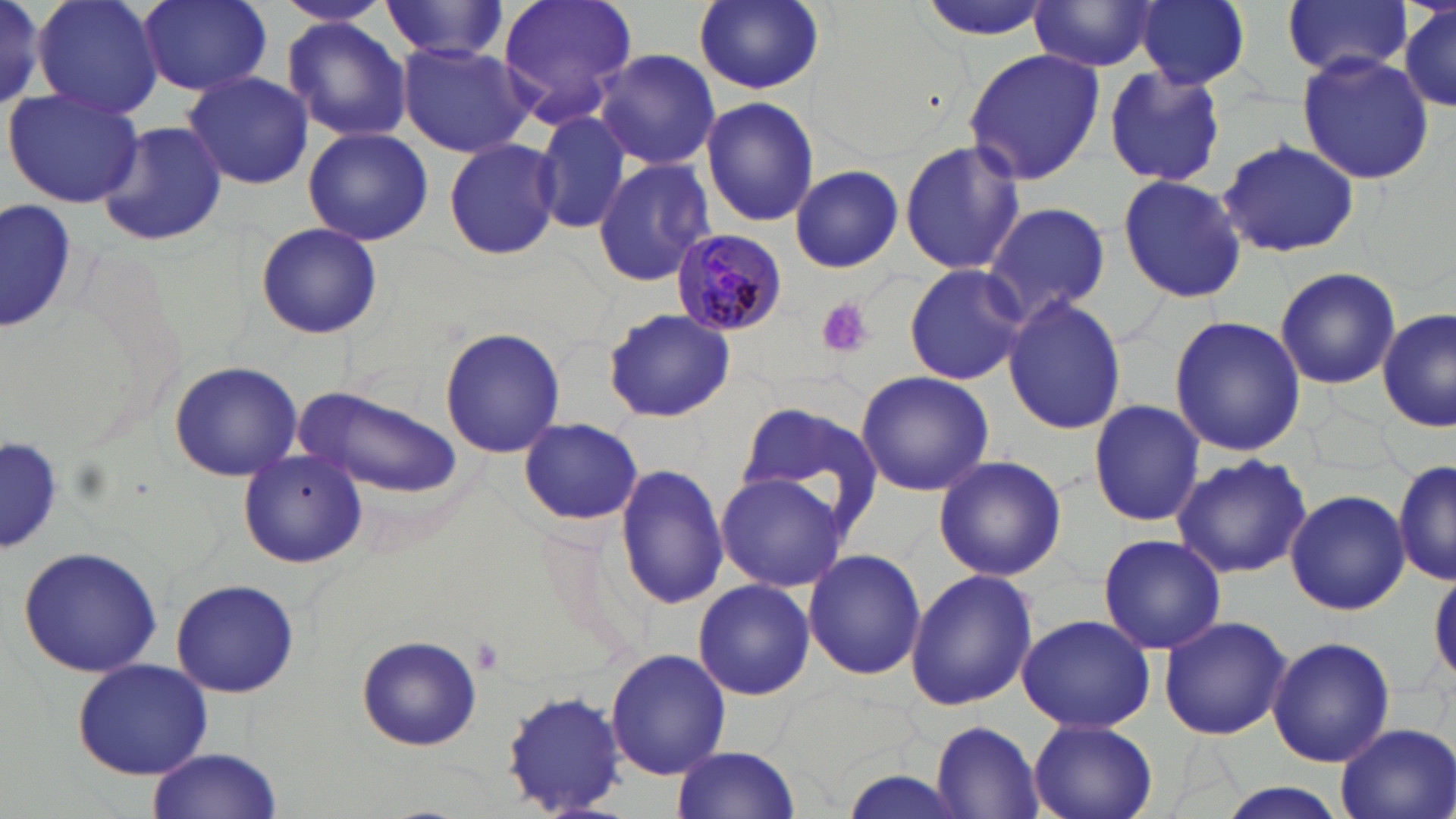 Approximate bounding boxes as [x1, y1, x2, y2] in pixels. Plasmodium malariae-infected red blood cell locations: [669, 230, 788, 338]. Uninfected red blood cell locations: [35, 0, 163, 121], [138, 0, 272, 95], [272, 0, 394, 31], [498, 0, 638, 128], [691, 0, 826, 97], [915, 0, 1059, 42], [1137, 0, 1250, 89], [1283, 0, 1410, 81], [0, 1, 49, 106], [0, 1, 56, 114], [1397, 1, 1455, 115], [379, 2, 511, 61], [1029, 2, 1161, 73], [281, 19, 414, 142], [395, 40, 535, 159], [594, 48, 721, 170], [961, 49, 1104, 183], [1295, 53, 1434, 184], [1102, 65, 1228, 189], [183, 69, 313, 190], [4, 88, 145, 208], [699, 97, 819, 228], [533, 106, 632, 235], [97, 121, 229, 248], [302, 127, 434, 246], [443, 137, 561, 263], [898, 139, 1025, 277], [1217, 141, 1359, 257], [592, 157, 715, 286], [789, 164, 903, 273], [1117, 173, 1248, 305], [2, 199, 78, 335], [981, 202, 1111, 324], [255, 222, 382, 340], [902, 263, 1031, 386], [1274, 266, 1401, 390], [1002, 296, 1128, 434], [601, 308, 735, 423], [1377, 310, 1453, 432], [1169, 315, 1307, 456], [439, 326, 564, 458], [167, 360, 303, 482], [855, 371, 993, 498], [296, 384, 463, 499], [1089, 399, 1205, 528], [733, 400, 884, 536], [518, 416, 643, 527], [2, 431, 66, 557], [235, 449, 368, 569], [1171, 454, 1314, 578], [933, 455, 1066, 581], [615, 461, 729, 609], [1394, 461, 1455, 588], [714, 472, 849, 593], [1284, 487, 1409, 615], [1095, 535, 1228, 655], [16, 545, 163, 678], [803, 548, 926, 681], [1430, 563, 1456, 688], [905, 568, 1039, 711], [692, 579, 815, 700], [170, 580, 298, 697], [1015, 613, 1157, 734], [1159, 614, 1292, 740], [357, 635, 482, 751], [1267, 636, 1395, 767], [605, 648, 731, 780], [73, 658, 215, 780], [501, 688, 628, 818], [1028, 719, 1157, 819], [929, 721, 1044, 817], [1332, 722, 1455, 819], [670, 745, 802, 817], [146, 749, 282, 819], [835, 770, 968, 819], [1211, 782, 1355, 819]. Platelet locations: [815, 297, 873, 358], [472, 636, 503, 674]. Slide-level diagnosis: Plasmodium malariae. Captured at 1000x magnification. May-Grünwald-Giemsa stain. Optical microscopy. Thin blood film. Single field of view. Image is 1456×819 pixels.